Report the malaria status of this cell.
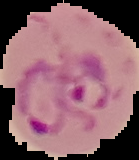
It is parasitized.

From a thin blood film. Image is 139×160 pixels. Cell region segmented out of the field of view; the surrounding area is masked to black.